Report the malaria status of this cell.
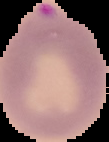

It is parasitized.

image type = segmented cell region with the area outside set to black
preparation = thin blood smear
image size = 109×142 pixels